State the preparation type.
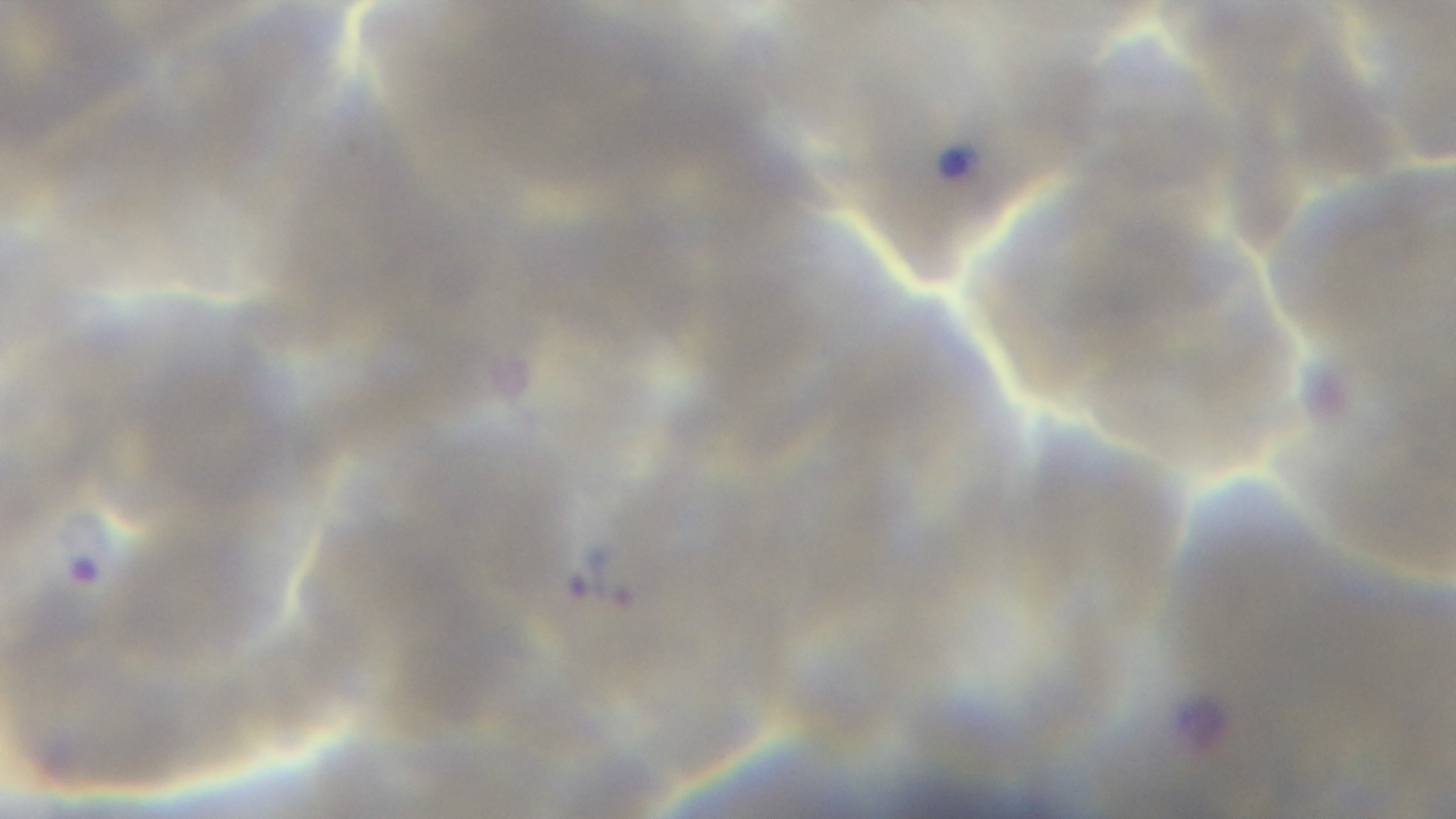
A thin smear.

Summary:
  - Stain: Giemsa
  - Capture: mounted 4K digital camera
  - Field of view: single
  - Malaria status: infected
  - Objective: 100x oil immersion
  - Modality: light microscopy